Classify the preparation.
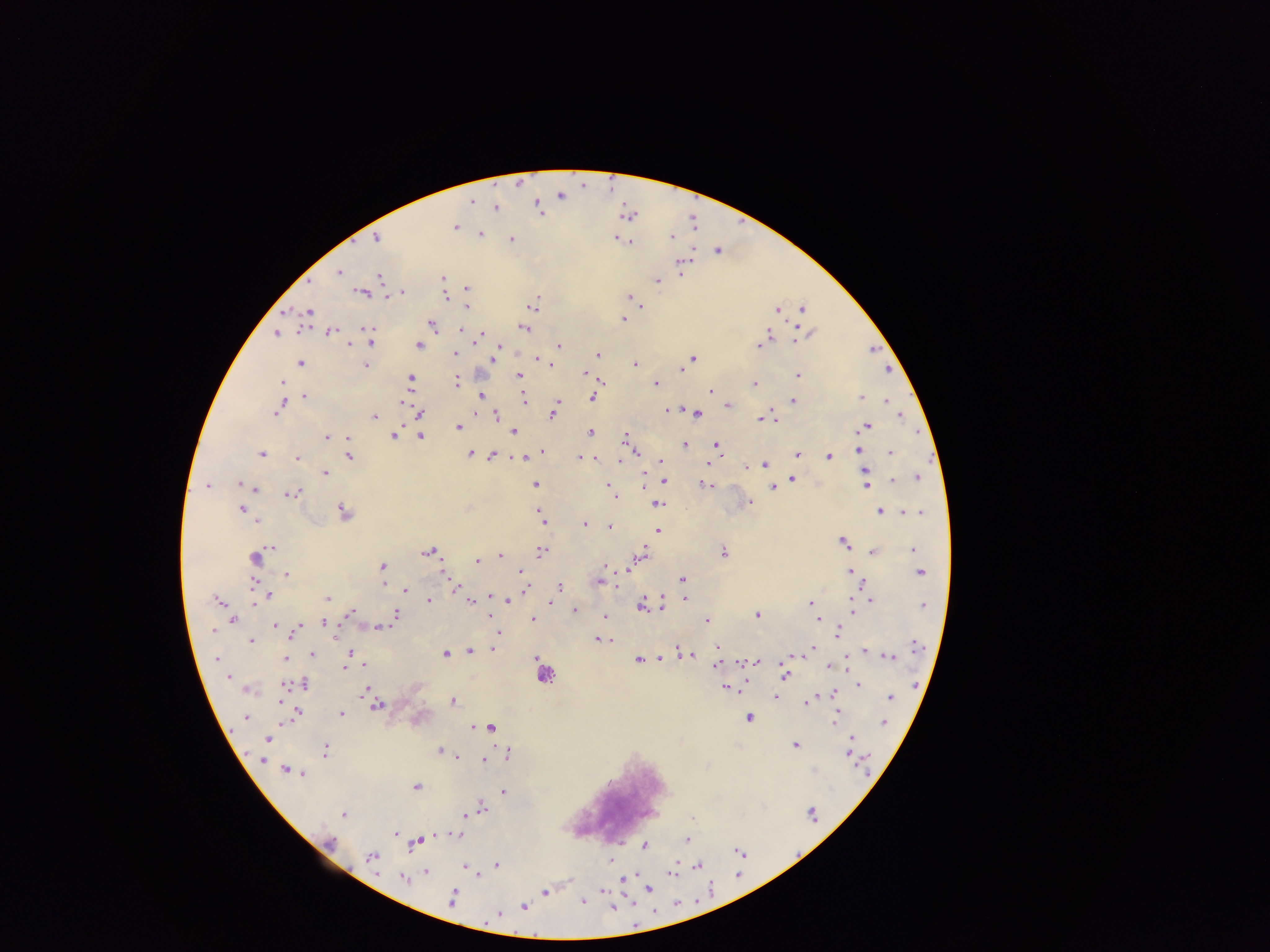
Thick blood film.

Approximate centers as [x, y] in pixels.
Summary:
  - Plasmodium parasite locations: [518, 182], [560, 196], [472, 200], [537, 205], [495, 208], [539, 211], [627, 216], [455, 226], [479, 234], [671, 236], [376, 238], [616, 238], [625, 239], [511, 240], [629, 241], [718, 250], [680, 264], [338, 272], [378, 276], [441, 279], [656, 282], [465, 288], [402, 291], [362, 292], [445, 295], [386, 296], [629, 298], [532, 303], [466, 306], [639, 307], [802, 308], [777, 311], [308, 314], [623, 319], [433, 325], [523, 327], [364, 329], [462, 330], [276, 332], [330, 332], [479, 335], [795, 339], [369, 340], [417, 344], [349, 345], [757, 345], [558, 346], [498, 347], [454, 354], [598, 354], [692, 358], [538, 360], [492, 361], [300, 363], [635, 363], [549, 364], [365, 365], [683, 365], [679, 369], [584, 375], [518, 376], [797, 376], [410, 379], [455, 381], [281, 383], [655, 384], [755, 384], [710, 391], [305, 395], [479, 395], [592, 397], [861, 398], [524, 399], [792, 400], [402, 401], [886, 401], [280, 406], [726, 406], [667, 410], [420, 413], [552, 413], [696, 415], [900, 415], [375, 416], [496, 416], [770, 416], [760, 419], [865, 426], [458, 427], [513, 431], [590, 432], [393, 434], [420, 435], [325, 437], [346, 438], [625, 438], [684, 444], [716, 446], [543, 451], [858, 451], [474, 452], [260, 453], [469, 453], [637, 453], [890, 453], [796, 454], [491, 455], [348, 456], [520, 456], [828, 456], [297, 457], [578, 458], [596, 459], [620, 460], [661, 461], [709, 462], [765, 465], [746, 467], [864, 471], [323, 472], [791, 478], [917, 478], [891, 480], [663, 481], [242, 484], [535, 485], [608, 485], [706, 485], [865, 485], [207, 486], [772, 487], [253, 488], [292, 492], [610, 492], [613, 497], [748, 502], [657, 504], [242, 509], [880, 511], [904, 511], [342, 512], [919, 512], [257, 520], [542, 521], [583, 524], [608, 526], [657, 531], [843, 542], [273, 547], [912, 549], [428, 551], [541, 551], [873, 551], [723, 553], [643, 554], [500, 555], [916, 555], [254, 557], [477, 561], [382, 566], [607, 567], [630, 567], [849, 571], [521, 572], [919, 573], [286, 574], [444, 574], [681, 579], [598, 582], [254, 584], [862, 584], [524, 587], [559, 587], [455, 588], [405, 590], [267, 596], [262, 598], [478, 598], [328, 599], [506, 599], [685, 599], [429, 600], [471, 600], [871, 600], [218, 602], [810, 603], [852, 603], [551, 604], [641, 604], [661, 607], [923, 607], [574, 609], [852, 611], [350, 613], [395, 614], [606, 615], [756, 615], [533, 618], [818, 619], [233, 620], [706, 621], [323, 622], [275, 625], [379, 627], [212, 630], [498, 632], [836, 632], [292, 635], [338, 635], [598, 639], [251, 640], [914, 646], [717, 647], [493, 648], [811, 648], [469, 651], [864, 651], [679, 652], [809, 652], [313, 653], [352, 653], [446, 654], [691, 655], [786, 655], [803, 655], [889, 656], [537, 658], [659, 658], [697, 658], [285, 659], [217, 660], [638, 660], [743, 661], [757, 662], [363, 664], [715, 665], [845, 666], [345, 667], [784, 674], [227, 675], [303, 683], [282, 684], [857, 684], [742, 686], [416, 687], [365, 688], [725, 688], [249, 690], [776, 694], [833, 694], [774, 696], [891, 696], [452, 701], [283, 702], [805, 702], [376, 706], [296, 711], [836, 711], [341, 713], [246, 718], [749, 718], [884, 722], [834, 724], [473, 725], [490, 727], [851, 737], [268, 739], [795, 744], [325, 750], [439, 750], [507, 751], [849, 756], [456, 757], [261, 759], [483, 759], [285, 769], [292, 771], [300, 771], [415, 787], [503, 791], [482, 809], [344, 814], [464, 814], [692, 819], [394, 834], [457, 835], [435, 836], [686, 839], [415, 842], [329, 843], [645, 845], [372, 857], [611, 860], [496, 866], [697, 866], [464, 867], [426, 871], [474, 872], [675, 872], [477, 876], [401, 879], [649, 889], [602, 891], [545, 892], [453, 894], [452, 899], [582, 901], [523, 907], [496, 914]
  - Leukocyte locations: [543, 674]
  - Country: Ghana
  - Capture: mobile-phone photograph through a microscope
  - Image size: 1270×952 pixels
  - Field of view: single